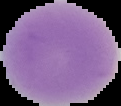
Cell region segmented out of the field of view; the surrounding area is masked to black. Image is 121×106 pixels. From a thin blood smear. Malaria status: uninfected.